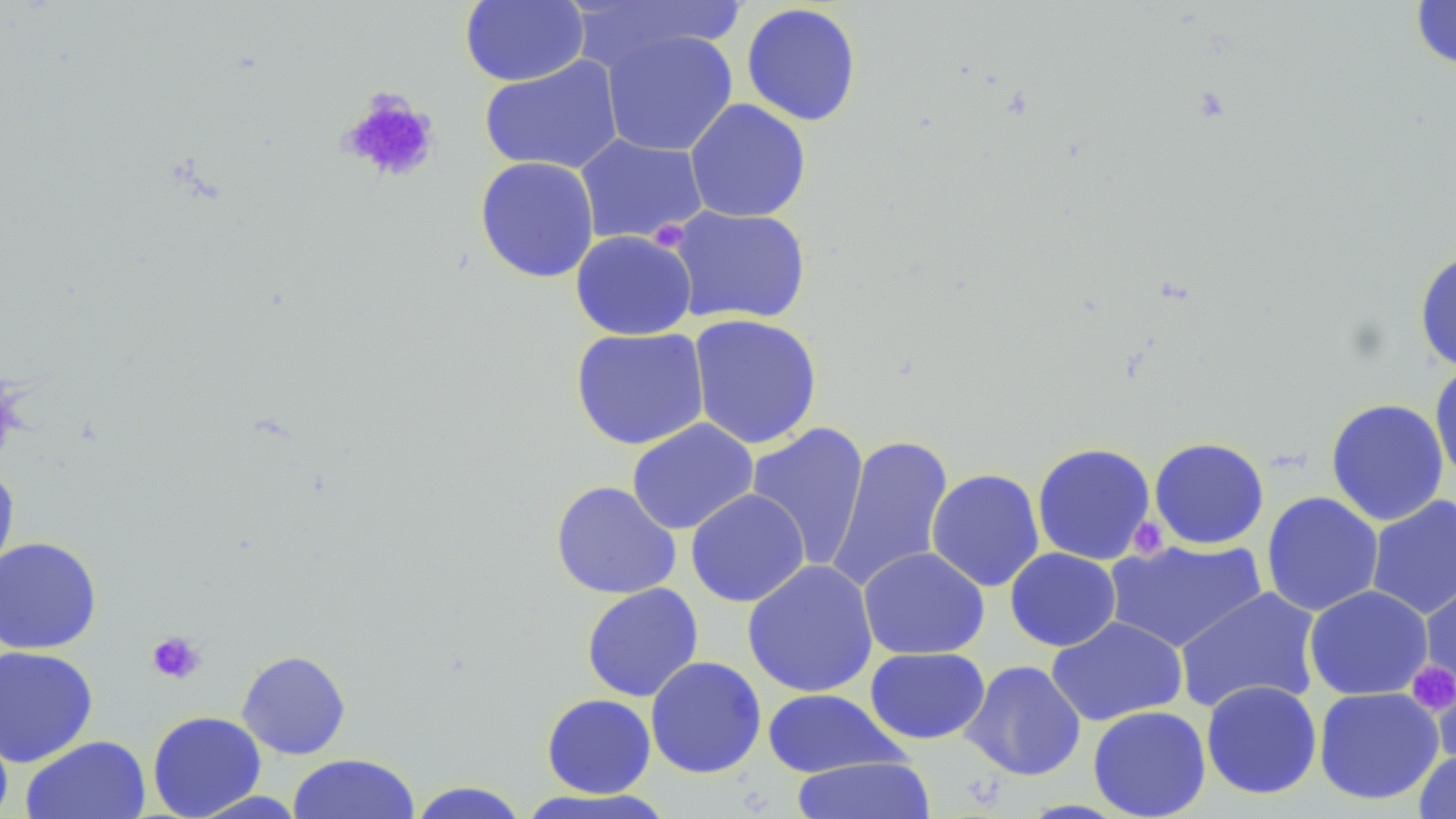
Summary:
  - Coordinate format: approximate bounding boxes as named x1/y1/x2/y2 corners in pixels
  - Platelet locations: (x1=337, y1=89, x2=440, y2=184), (x1=1128, y1=516, x2=1168, y2=560), (x1=146, y1=631, x2=206, y2=685), (x1=1407, y1=660, x2=1455, y2=716)
  - Uninfected red blood cell locations: (x1=459, y1=0, x2=589, y2=86), (x1=1410, y1=0, x2=1456, y2=71), (x1=572, y1=1, x2=746, y2=73), (x1=741, y1=3, x2=862, y2=127), (x1=601, y1=29, x2=738, y2=157), (x1=479, y1=55, x2=624, y2=175), (x1=684, y1=98, x2=811, y2=223), (x1=574, y1=134, x2=709, y2=245), (x1=475, y1=156, x2=600, y2=283), (x1=667, y1=205, x2=812, y2=326), (x1=570, y1=230, x2=697, y2=340), (x1=1414, y1=248, x2=1456, y2=374), (x1=687, y1=314, x2=823, y2=450), (x1=570, y1=327, x2=711, y2=450), (x1=1429, y1=359, x2=1456, y2=488), (x1=1325, y1=398, x2=1450, y2=526), (x1=626, y1=418, x2=759, y2=535), (x1=745, y1=421, x2=870, y2=570), (x1=826, y1=434, x2=955, y2=594), (x1=1148, y1=436, x2=1269, y2=550), (x1=1032, y1=442, x2=1157, y2=565), (x1=0, y1=461, x2=20, y2=589), (x1=926, y1=468, x2=1045, y2=591), (x1=550, y1=480, x2=682, y2=600), (x1=685, y1=488, x2=810, y2=607), (x1=1261, y1=491, x2=1384, y2=617), (x1=1365, y1=495, x2=1456, y2=621), (x1=0, y1=536, x2=102, y2=655), (x1=1104, y1=539, x2=1268, y2=654), (x1=858, y1=546, x2=990, y2=660), (x1=1004, y1=547, x2=1121, y2=651), (x1=742, y1=559, x2=879, y2=698), (x1=1419, y1=577, x2=1456, y2=703), (x1=581, y1=583, x2=704, y2=702), (x1=1304, y1=584, x2=1433, y2=701), (x1=1174, y1=587, x2=1323, y2=714), (x1=1046, y1=616, x2=1188, y2=726), (x1=0, y1=645, x2=99, y2=768), (x1=864, y1=647, x2=990, y2=745), (x1=236, y1=650, x2=351, y2=759), (x1=645, y1=656, x2=767, y2=779), (x1=960, y1=660, x2=1087, y2=781), (x1=1432, y1=667, x2=1456, y2=765), (x1=1200, y1=680, x2=1323, y2=799), (x1=1313, y1=686, x2=1444, y2=805), (x1=762, y1=688, x2=908, y2=777), (x1=541, y1=693, x2=656, y2=798), (x1=1088, y1=705, x2=1211, y2=818), (x1=147, y1=710, x2=266, y2=818), (x1=0, y1=715, x2=14, y2=819), (x1=21, y1=735, x2=152, y2=819), (x1=1413, y1=748, x2=1456, y2=818), (x1=287, y1=753, x2=421, y2=818), (x1=789, y1=756, x2=937, y2=818), (x1=407, y1=781, x2=530, y2=819), (x1=516, y1=788, x2=675, y2=818)
  - Slide-level diagnosis: negative for blood parasites
  - Image size: 1456×819 pixels
  - Modality: light microscopy
  - Preparation: thin blood film
  - Field of view: single
  - Stain: May-Grünwald-Giemsa
  - Magnification: 1000x